Point out each leukocyte.
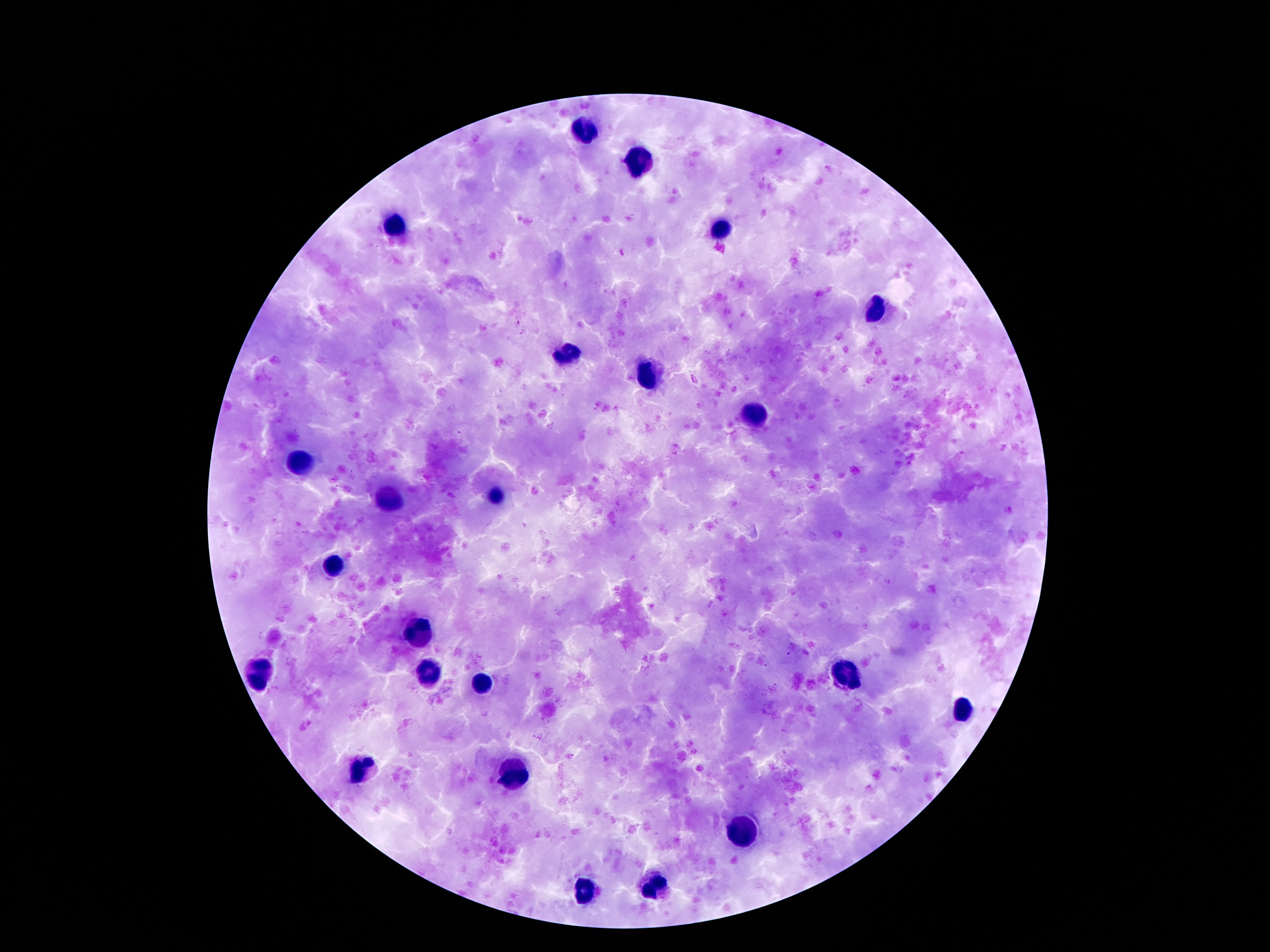

Approximate object centers, in pixels from the top-left corner.
Leukocytes: (x=581, y=130), (x=637, y=165), (x=396, y=225), (x=721, y=228), (x=875, y=310), (x=568, y=354), (x=646, y=377), (x=755, y=409), (x=301, y=463), (x=495, y=496), (x=388, y=501), (x=333, y=565), (x=421, y=633), (x=428, y=672), (x=258, y=675), (x=843, y=676), (x=480, y=686), (x=963, y=709), (x=358, y=766), (x=509, y=776), (x=744, y=833), (x=660, y=886), (x=585, y=892).

{
  "stain": "Giemsa",
  "preparation": "thick blood film",
  "patient_malaria_status": "negative",
  "capture": "smartphone camera through the microscope eyepiece",
  "field_of_view": "one from this slide",
  "magnification": "100x",
  "image_size": "1270×952 pixels"
}